State which cell type is depicted.
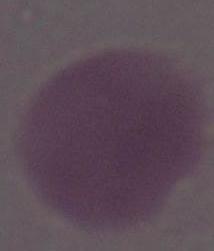

An erythrocyte.

modality: photomicrograph
magnification: 1000x